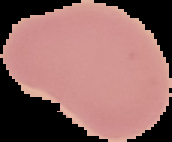
Summary:
  - Image size: 172×142 pixels
  - Image type: cell region segmented out of the field of view; surrounding area masked to black
  - Preparation: thin blood smear
  - Result: no Plasmodium parasites detected